Locate every Plasmodium parasite and every leukocyte.
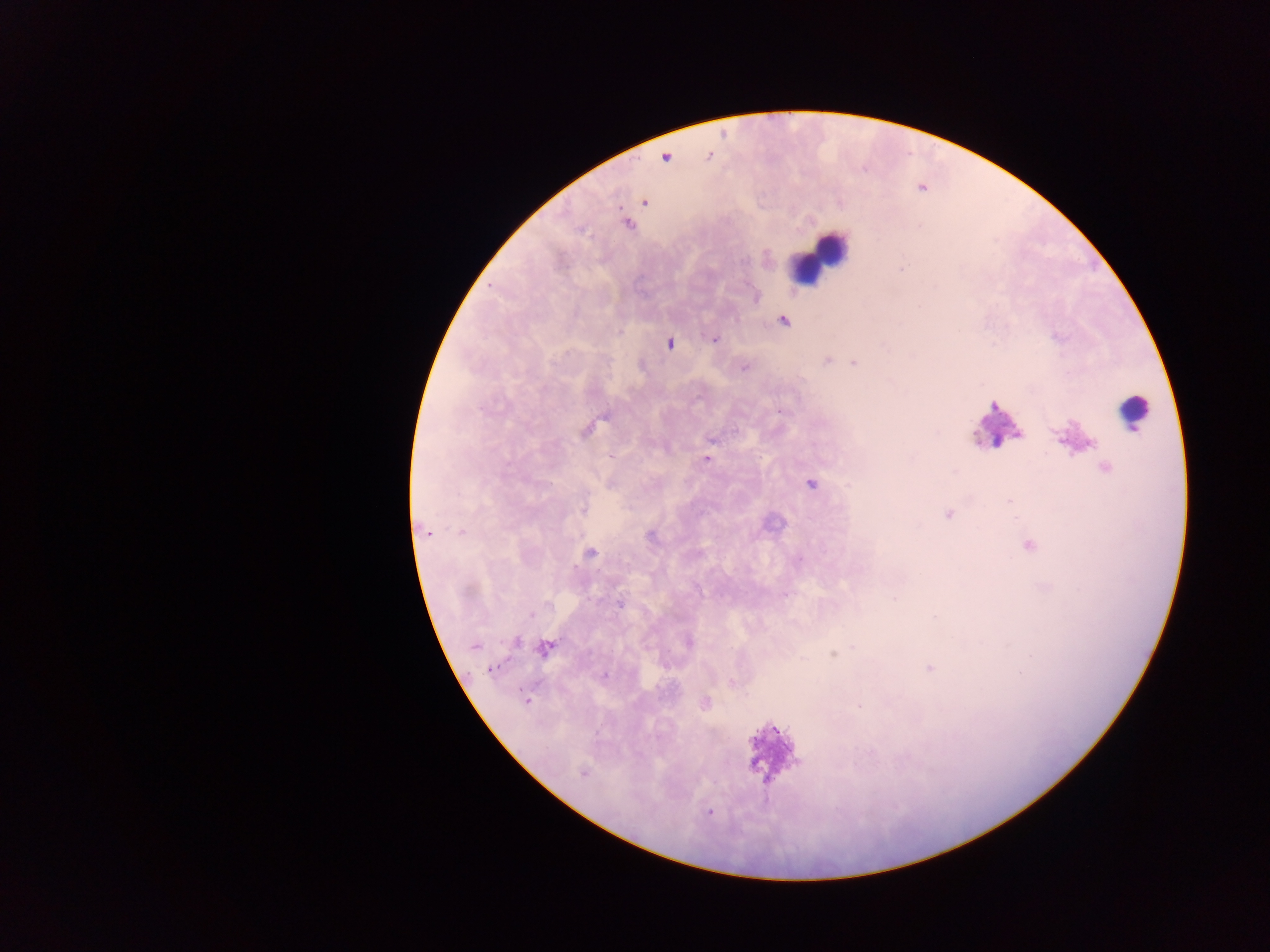
Approximate centers as (x, y) in pixels.
Plasmodium parasites: (709, 155), (666, 158), (644, 202), (627, 224), (782, 320), (714, 339), (669, 342), (827, 359), (855, 362), (744, 366), (780, 409), (587, 428), (706, 459), (1104, 467), (811, 484), (583, 508), (948, 513), (427, 531), (651, 534), (1027, 545), (590, 553), (620, 603), (516, 641), (688, 642), (474, 646), (545, 647), (834, 653), (930, 668), (491, 669), (604, 675), (733, 682), (525, 701), (704, 702), (859, 708), (582, 773), (709, 812).
Leukocytes: (819, 257), (1133, 411), (994, 426), (770, 754).

Image is 1270×952 pixels. One field of view. Thick blood film. Mobile-phone photograph taken through the microscope. Sample from Ghana.